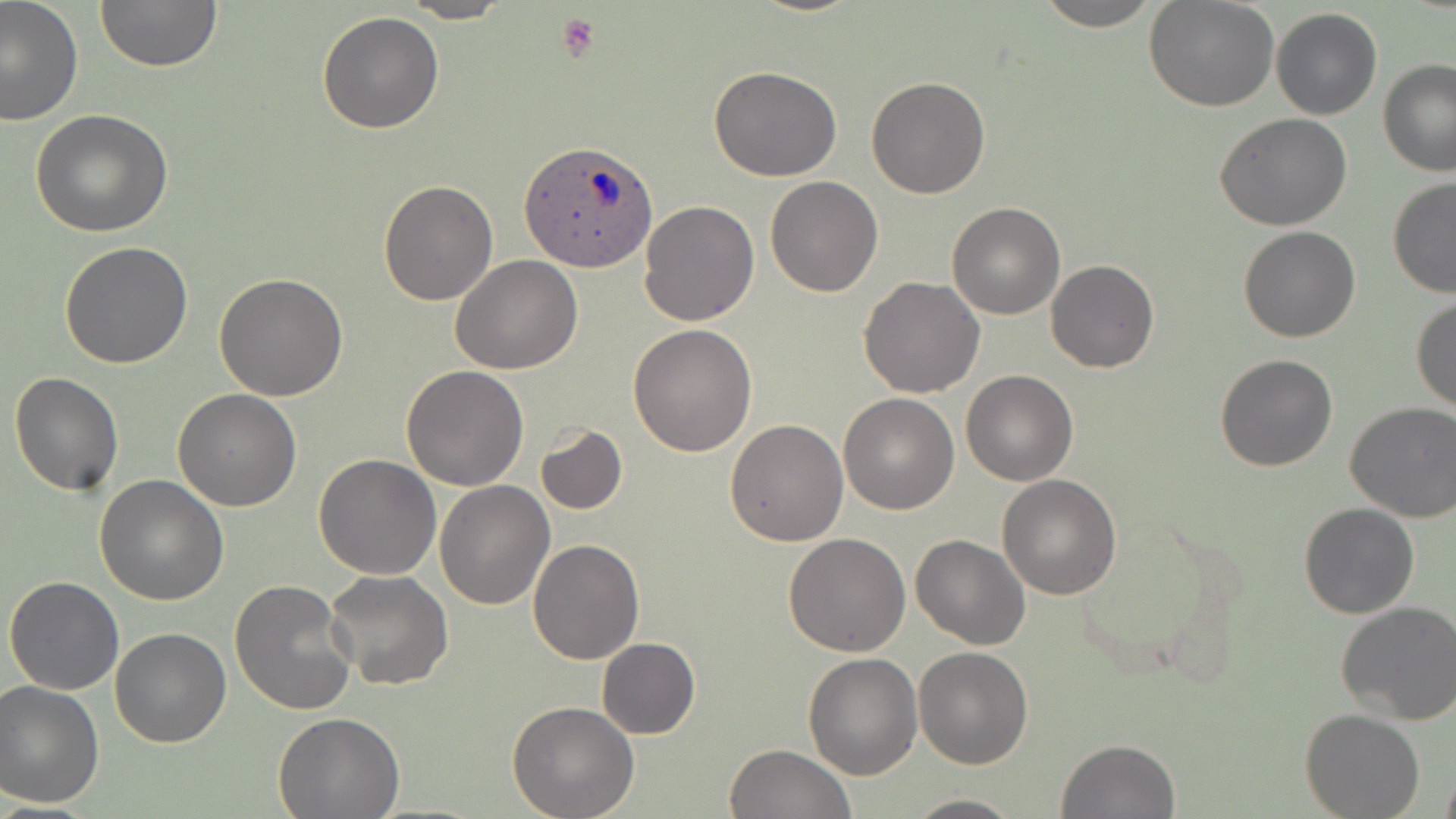

slide-level diagnosis = Plasmodium ovale
field of view = single
stain = May-Grünwald-Giemsa
platelet locations = approximate bounding boxes as (x1, y1, x2, y2) in pixels: (554, 11, 599, 62)
Plasmodium ovale-infected red blood cell locations = approximate bounding boxes as (x1, y1, x2, y2) in pixels: (521, 141, 655, 273)
preparation = thin blood film
magnification = 1000x
uninfected red blood cell locations = approximate bounding boxes as (x1, y1, x2, y2) in pixels: (0, 0, 83, 126), (399, 0, 512, 23), (1033, 0, 1163, 31), (94, 1, 223, 73), (1145, 1, 1278, 112), (1271, 7, 1382, 121), (317, 11, 444, 134), (1378, 60, 1456, 177), (710, 66, 842, 183), (866, 76, 990, 199), (29, 110, 173, 238), (1214, 113, 1353, 229), (764, 176, 884, 296), (378, 178, 498, 304), (1387, 178, 1456, 299), (639, 199, 761, 326), (946, 201, 1065, 320), (1239, 226, 1361, 343), (60, 240, 194, 369), (450, 255, 584, 374), (1044, 259, 1159, 373), (214, 273, 348, 400), (857, 277, 985, 397), (1410, 295, 1456, 415), (627, 324, 758, 457), (1214, 353, 1339, 472), (401, 364, 530, 491), (960, 370, 1077, 486), (9, 372, 123, 495), (174, 389, 302, 511), (838, 393, 959, 515), (1344, 400, 1456, 522), (725, 419, 848, 546), (534, 425, 627, 514), (312, 454, 441, 578), (95, 474, 228, 606), (998, 475, 1122, 600), (435, 480, 556, 609), (1299, 503, 1420, 619), (784, 533, 911, 657), (911, 534, 1031, 649), (528, 537, 645, 664), (325, 569, 453, 692), (4, 575, 125, 695), (229, 579, 357, 716), (1335, 601, 1456, 724), (110, 628, 231, 747), (597, 638, 700, 738), (914, 646, 1034, 769), (802, 651, 923, 779), (0, 680, 105, 808), (506, 701, 640, 819), (274, 710, 403, 818), (1300, 710, 1424, 819), (1056, 739, 1180, 818), (725, 743, 854, 819), (1439, 762, 1456, 819), (901, 793, 1026, 818)
image size = 1456×819 pixels
modality = light microscopy